Give the extent of all Plasmodium malariae-infected red blood cells.
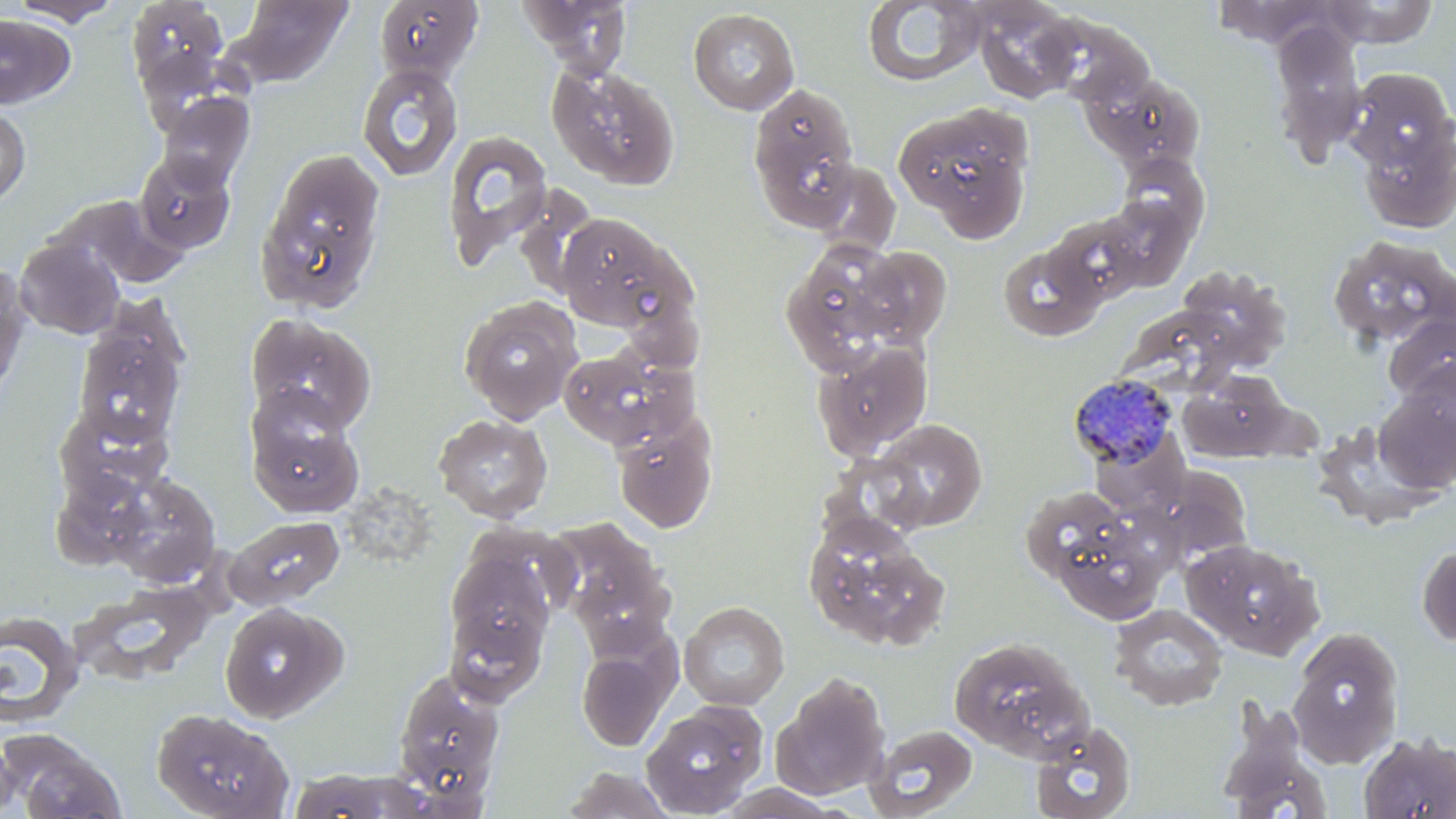

Approximate bounding boxes as [x1, y1, x2, y2] in pixels.
Plasmodium malariae-infected red blood cells: [1069, 373, 1179, 469].

Summary:
  - Uninfected red blood cell locations: [8, 0, 125, 26], [127, 0, 232, 101], [519, 0, 633, 74], [1212, 0, 1339, 49], [1321, 0, 1438, 47], [225, 1, 354, 87], [862, 1, 986, 87], [971, 1, 1082, 103], [688, 8, 800, 114], [1036, 11, 1157, 110], [0, 14, 76, 109], [1269, 23, 1367, 163], [356, 62, 464, 182], [547, 63, 680, 190], [1343, 67, 1456, 174], [1087, 73, 1206, 171], [748, 81, 861, 229], [155, 90, 255, 190], [893, 104, 1031, 233], [0, 105, 31, 208], [1355, 121, 1456, 234], [441, 130, 554, 272], [254, 147, 387, 315], [134, 152, 236, 255], [1117, 153, 1210, 240], [50, 194, 188, 291], [1098, 196, 1195, 290], [556, 212, 681, 330], [1047, 214, 1144, 305], [1326, 234, 1456, 350], [14, 236, 125, 340], [998, 242, 1105, 343], [796, 243, 927, 370], [852, 246, 952, 347], [0, 265, 31, 393], [1179, 265, 1292, 369], [458, 295, 582, 424], [245, 313, 377, 434], [1383, 313, 1456, 404], [73, 318, 188, 447], [814, 340, 932, 459], [558, 347, 696, 451], [1396, 358, 1456, 458], [1180, 371, 1290, 461], [1374, 385, 1456, 494], [247, 404, 364, 519], [55, 407, 173, 503], [433, 413, 553, 523], [1314, 416, 1447, 529], [866, 419, 988, 533], [614, 420, 717, 533], [1136, 469, 1263, 557], [50, 471, 174, 569], [111, 474, 220, 586], [342, 483, 449, 565], [1023, 489, 1115, 566], [802, 513, 949, 651], [226, 516, 345, 609], [545, 517, 676, 646], [1056, 532, 1164, 623], [1182, 538, 1323, 658], [444, 542, 559, 694], [1416, 543, 1456, 649], [71, 588, 213, 684], [679, 601, 790, 711], [220, 602, 347, 723], [1108, 603, 1229, 711], [0, 612, 83, 729], [1287, 625, 1404, 767], [948, 635, 1094, 761], [576, 640, 676, 752], [390, 666, 505, 804], [773, 672, 891, 800], [640, 699, 769, 817], [1215, 701, 1333, 818], [151, 707, 293, 819], [1028, 720, 1137, 819], [865, 723, 979, 818], [3, 730, 125, 819], [1358, 732, 1456, 819], [0, 733, 20, 818], [560, 767, 678, 818], [711, 783, 846, 818]
  - Slide-level diagnosis: Plasmodium malariae
  - Field of view: one of a larger specimen
  - Modality: optical microscopy
  - Preparation: thin blood film
  - Stain: May-Grünwald-Giemsa
  - Image size: 1456×819 pixels
  - Magnification: 1000x